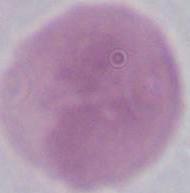

modality = photomicrograph
identification = erythrocyte
magnification = 1000x